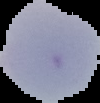
Summary:
  - Image type: cell region segmented out of the field of view; surrounding area masked to black
  - Preparation: thin blood smear
  - Result: negative for malaria parasites
  - Image size: 100×103 pixels